Name the parasite shown.
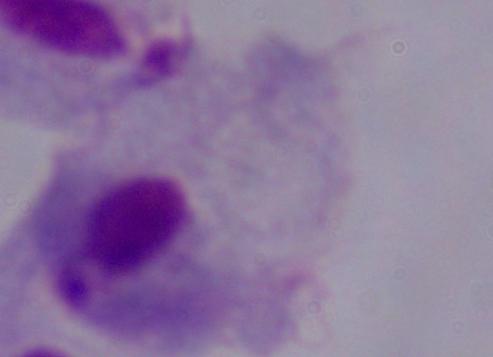
This is a trichomonad.

magnification = 1000x
modality = photomicrograph